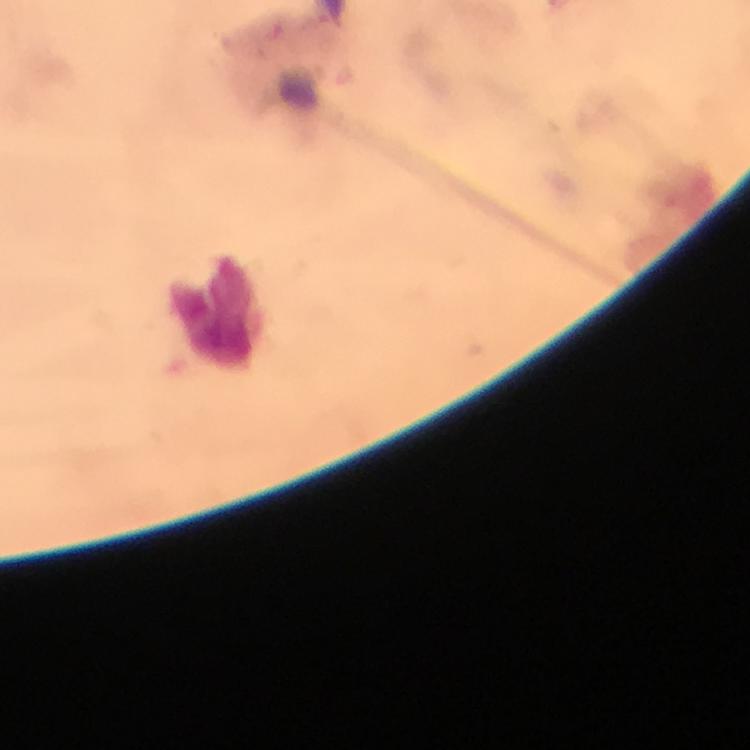

image size = 750×750 pixels
capture = smartphone camera through the microscope
context = from a malaria diagnostic workup
cropped from = a single field of view
immersion oil = used
magnification = 100x
Plasmodium parasites = none detected
preparation = thick blood film
leukocyte locations = approximate centers as [x, y] in pixels: [214, 311]
stain = Giemsa